Assess this cell for malaria.
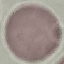
Uninfected.

Summary:
  - Capture: smartphone camera at the microscope eyepiece
  - Preparation: thin blood film
  - Image type: automatically extracted cell patch, resized to 64 × 64 pixels
  - Stain: Giemsa